Assess this cell for malaria.
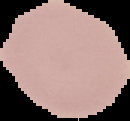

Uninfected.

From a thin blood film. Image is 130×121 pixels. Cell region segmented out of the field of view; the surrounding area is masked to black.